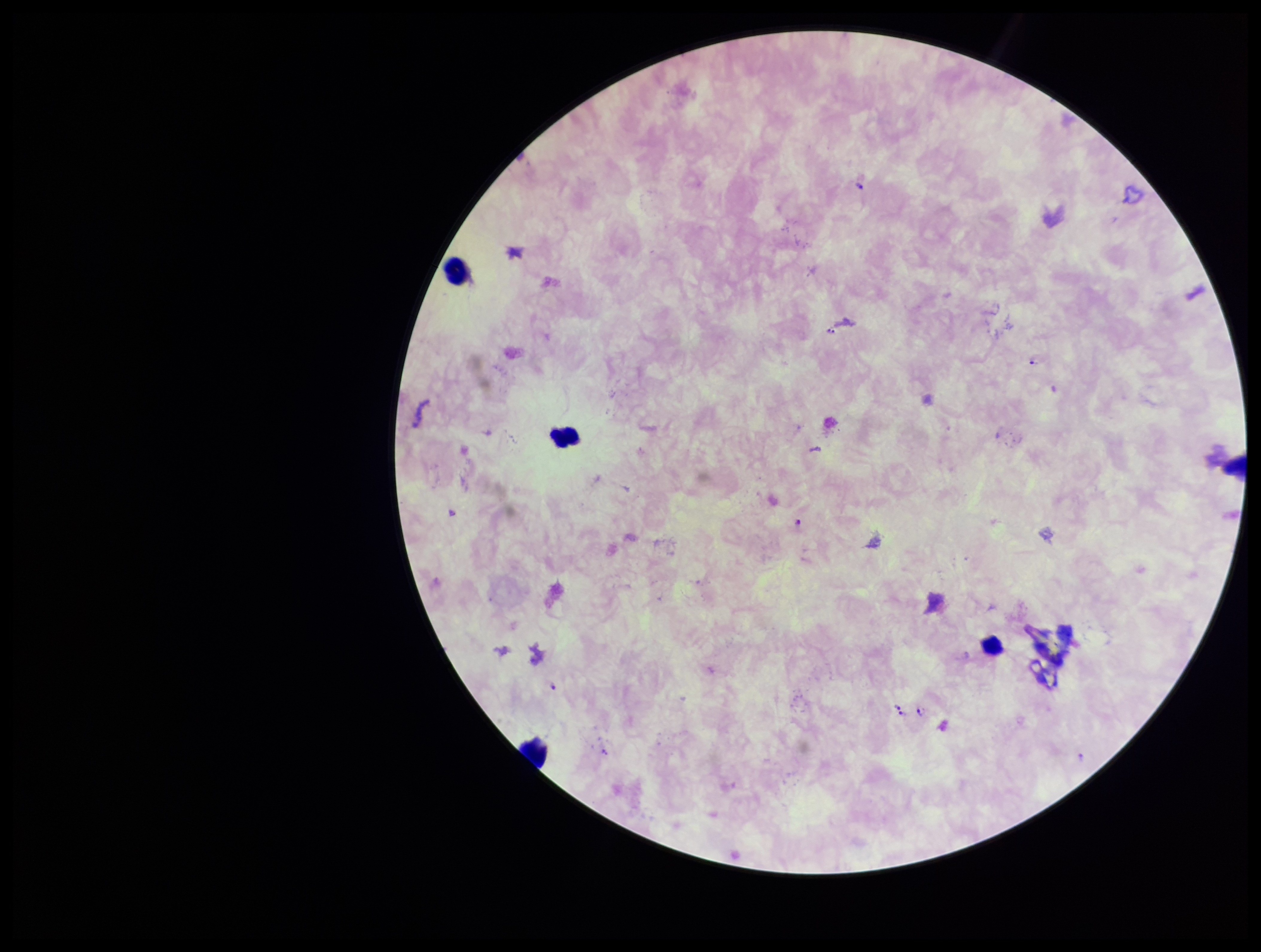
{
  "preparation": "thick smear",
  "species_reported_for_this_patient": "Plasmodium falciparum",
  "parasite_count": 7,
  "leukocyte_count": 5,
  "stain": "Giemsa",
  "image_size": "1261×952 pixels",
  "capture": "smartphone photograph through the microscope eyepiece",
  "patient_malaria_status": "infected",
  "field_of_view": "one from this slide",
  "plasmodium_parasites": "detected"
}